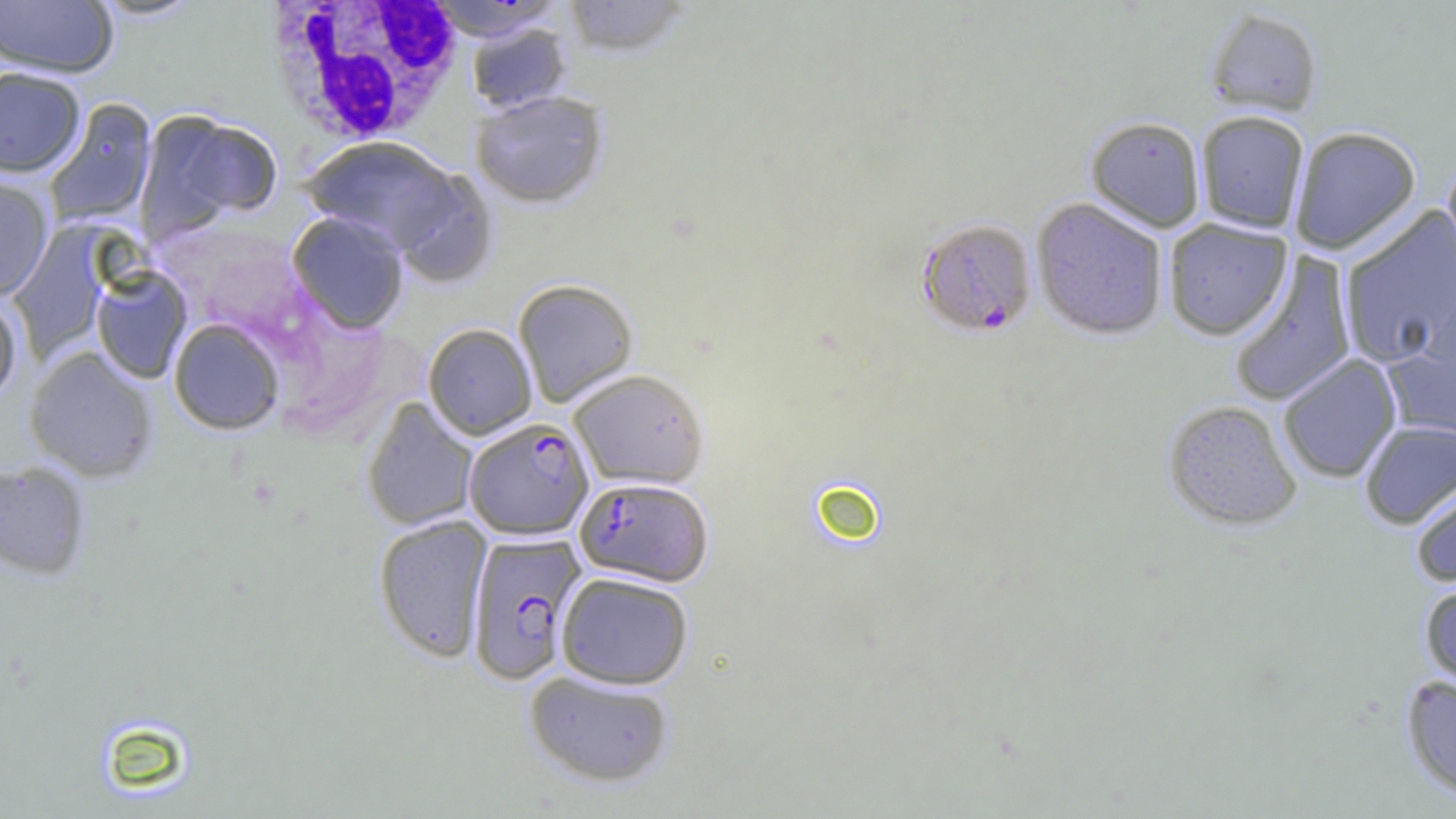
Summary:
  - Coordinate format: approximate bounding boxes as (x1, y1, x2, y2) in pixels
  - Uninfected red blood cell locations: (0, 0, 118, 78), (91, 0, 205, 21), (561, 0, 694, 59), (425, 1, 566, 42), (1204, 7, 1324, 120), (466, 23, 572, 114), (0, 66, 85, 178), (471, 90, 608, 208), (43, 99, 157, 227), (139, 112, 280, 236), (1195, 112, 1309, 234), (1085, 117, 1206, 233), (1290, 127, 1421, 255), (302, 136, 461, 254), (1440, 162, 1456, 285), (390, 169, 497, 288), (0, 174, 53, 301), (1030, 198, 1168, 342), (1338, 206, 1456, 368), (287, 212, 409, 334), (1163, 219, 1292, 341), (7, 225, 112, 361), (1228, 250, 1357, 407), (91, 267, 192, 383), (512, 278, 638, 408), (1419, 283, 1455, 409), (0, 293, 22, 404), (169, 319, 284, 435), (423, 323, 537, 440), (1381, 345, 1456, 446), (24, 347, 158, 482), (1278, 354, 1402, 484), (568, 369, 709, 490), (362, 397, 479, 532), (1163, 401, 1302, 532), (1359, 419, 1456, 530), (0, 461, 91, 580), (1410, 474, 1456, 588), (374, 514, 492, 663), (555, 572, 694, 689), (1420, 581, 1456, 692), (524, 670, 675, 787), (1401, 675, 1456, 800)
  - Plasmodium falciparum-infected red blood cell locations: (916, 219, 1038, 338), (464, 418, 594, 540), (575, 477, 713, 586), (466, 532, 587, 685)
  - White blood cell locations: (262, 0, 467, 140)
  - Slide-level diagnosis: Plasmodium falciparum
  - Modality: light microscopy
  - Preparation: thin blood smear
  - Magnification: 1000x
  - Field of view: single
  - Image size: 1456×819 pixels